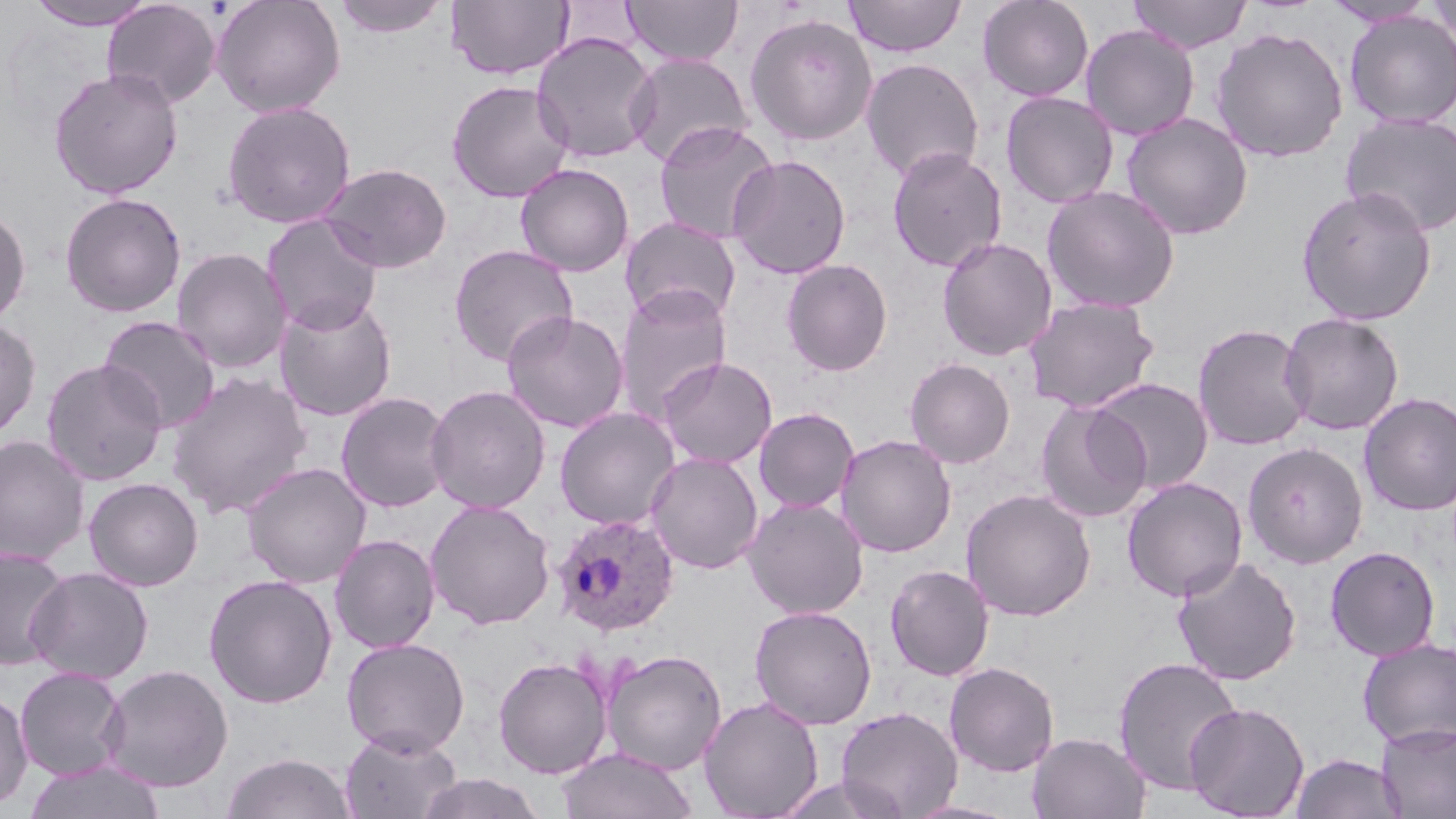

Plasmodium ovale-infected red blood cell locations = approximate bounding boxes as named x1/y1/x2/y2 corners in pixels: (x1=552, y1=513, x2=680, y2=636)
slide-level diagnosis = Plasmodium ovale
preparation = thin blood film
image size = 1456×819 pixels
uninfected red blood cell locations = approximate bounding boxes as named x1/y1/x2/y2 corners in pixels: (x1=24, y1=0, x2=160, y2=31), (x1=102, y1=0, x2=221, y2=109), (x1=211, y1=0, x2=346, y2=118), (x1=332, y1=0, x2=450, y2=38), (x1=447, y1=0, x2=575, y2=81), (x1=622, y1=0, x2=743, y2=66), (x1=844, y1=0, x2=966, y2=57), (x1=977, y1=0, x2=1094, y2=103), (x1=1128, y1=0, x2=1252, y2=54), (x1=1425, y1=0, x2=1456, y2=48), (x1=1321, y1=1, x2=1438, y2=28), (x1=1344, y1=11, x2=1456, y2=128), (x1=744, y1=13, x2=878, y2=146), (x1=1080, y1=24, x2=1199, y2=140), (x1=1210, y1=27, x2=1349, y2=163), (x1=531, y1=32, x2=660, y2=163), (x1=626, y1=53, x2=754, y2=168), (x1=860, y1=57, x2=984, y2=183), (x1=48, y1=67, x2=184, y2=199), (x1=446, y1=79, x2=575, y2=202), (x1=1000, y1=91, x2=1119, y2=208), (x1=221, y1=100, x2=356, y2=228), (x1=1120, y1=112, x2=1254, y2=240), (x1=1340, y1=112, x2=1456, y2=237), (x1=653, y1=121, x2=779, y2=245), (x1=886, y1=146, x2=1007, y2=272), (x1=727, y1=154, x2=851, y2=279), (x1=318, y1=163, x2=452, y2=273), (x1=515, y1=163, x2=634, y2=276), (x1=1041, y1=185, x2=1181, y2=313), (x1=1296, y1=185, x2=1438, y2=326), (x1=59, y1=191, x2=186, y2=318), (x1=0, y1=204, x2=31, y2=327), (x1=261, y1=214, x2=384, y2=335), (x1=620, y1=216, x2=742, y2=325), (x1=936, y1=237, x2=1057, y2=361), (x1=448, y1=244, x2=579, y2=368), (x1=171, y1=247, x2=292, y2=374), (x1=781, y1=258, x2=893, y2=376), (x1=614, y1=285, x2=732, y2=421), (x1=274, y1=295, x2=398, y2=422), (x1=1023, y1=296, x2=1160, y2=413), (x1=501, y1=309, x2=629, y2=433), (x1=1279, y1=312, x2=1405, y2=436), (x1=97, y1=315, x2=221, y2=434), (x1=0, y1=318, x2=41, y2=440), (x1=1192, y1=322, x2=1313, y2=451), (x1=656, y1=356, x2=778, y2=469), (x1=904, y1=358, x2=1015, y2=468), (x1=41, y1=359, x2=167, y2=486), (x1=167, y1=371, x2=313, y2=518), (x1=1090, y1=377, x2=1214, y2=493), (x1=425, y1=384, x2=551, y2=514), (x1=336, y1=391, x2=454, y2=512), (x1=1358, y1=392, x2=1456, y2=516), (x1=1034, y1=400, x2=1153, y2=523), (x1=555, y1=406, x2=681, y2=529), (x1=753, y1=408, x2=859, y2=512), (x1=835, y1=434, x2=957, y2=558), (x1=0, y1=435, x2=91, y2=566), (x1=1242, y1=441, x2=1368, y2=568), (x1=645, y1=452, x2=763, y2=574), (x1=241, y1=462, x2=371, y2=588), (x1=1121, y1=476, x2=1248, y2=601), (x1=83, y1=477, x2=204, y2=591), (x1=960, y1=488, x2=1097, y2=622), (x1=742, y1=497, x2=869, y2=619), (x1=425, y1=498, x2=556, y2=630), (x1=329, y1=534, x2=441, y2=654), (x1=1324, y1=545, x2=1441, y2=661), (x1=0, y1=546, x2=72, y2=670), (x1=1172, y1=556, x2=1302, y2=685), (x1=885, y1=564, x2=995, y2=681), (x1=25, y1=566, x2=154, y2=684), (x1=203, y1=574, x2=338, y2=708), (x1=749, y1=605, x2=877, y2=730), (x1=341, y1=637, x2=470, y2=757), (x1=1358, y1=638, x2=1456, y2=749), (x1=602, y1=649, x2=727, y2=775), (x1=492, y1=655, x2=613, y2=778), (x1=1112, y1=655, x2=1243, y2=796), (x1=944, y1=661, x2=1060, y2=777), (x1=99, y1=663, x2=234, y2=792), (x1=14, y1=666, x2=129, y2=781), (x1=0, y1=689, x2=33, y2=810), (x1=699, y1=695, x2=823, y2=818), (x1=1184, y1=701, x2=1310, y2=818), (x1=835, y1=705, x2=963, y2=819), (x1=1376, y1=722, x2=1456, y2=818), (x1=340, y1=728, x2=461, y2=818), (x1=1026, y1=731, x2=1151, y2=819), (x1=556, y1=747, x2=697, y2=819), (x1=221, y1=752, x2=355, y2=818), (x1=1290, y1=753, x2=1406, y2=818), (x1=21, y1=760, x2=168, y2=819), (x1=417, y1=771, x2=544, y2=818), (x1=774, y1=774, x2=907, y2=818), (x1=900, y1=799, x2=1023, y2=819)
magnification = 1000x
stain = May-Grünwald-Giemsa
field of view = one of a larger specimen
modality = optical microscopy